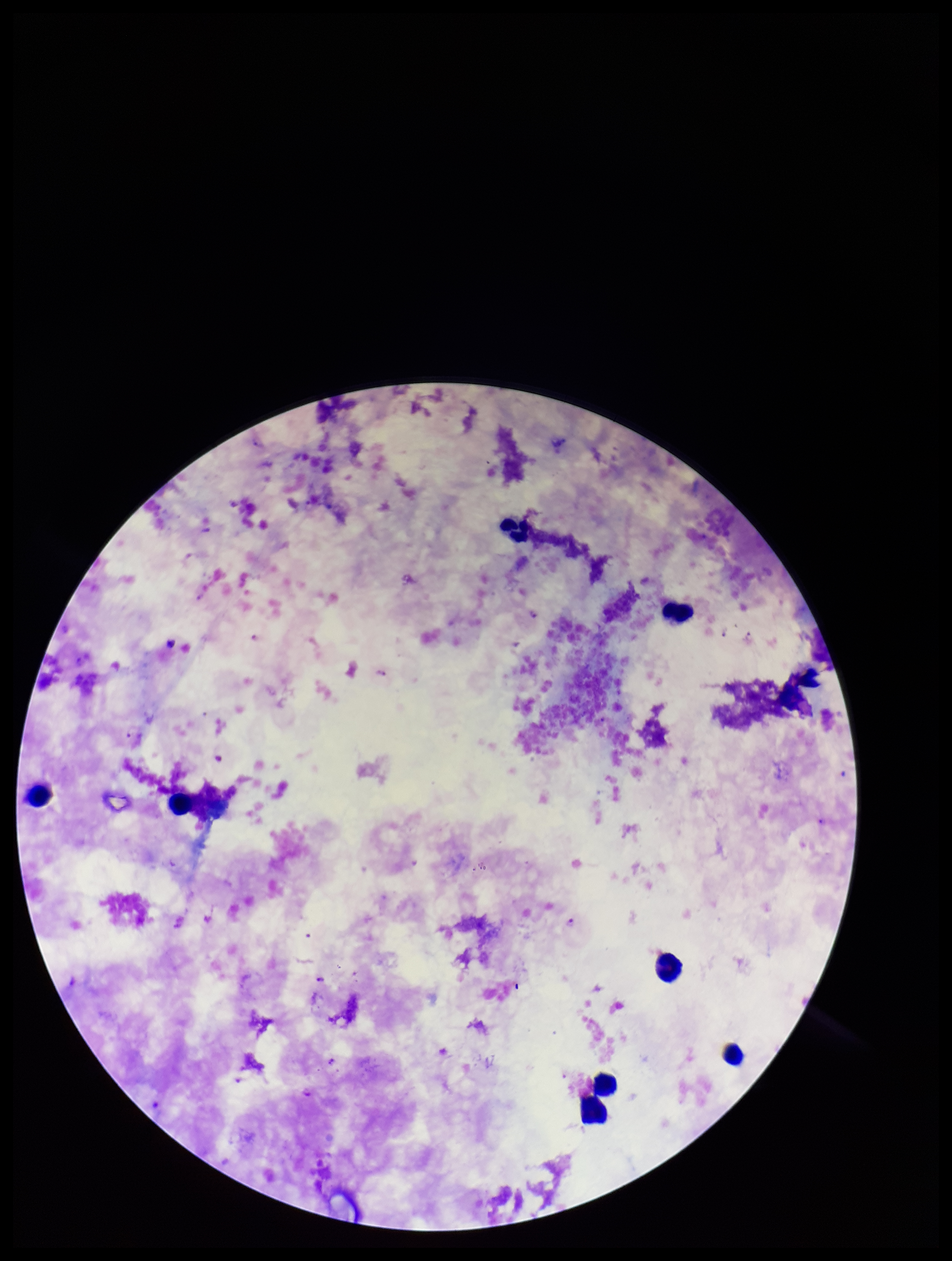
Image is 952×1261 pixels. Leukocyte count: 8. One field from this slide. Preparation: thick smear. Species reported for this patient: Plasmodium falciparum. Photographed through the microscope eyepiece with a smartphone camera. Giemsa stain. Plasmodium parasites: detected. Parasite count: 5. Patient malaria status: infected.